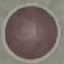

Summary:
  - Malaria status: uninfected
  - Capture: smartphone camera at the microscope eyepiece
  - Stain: Giemsa
  - Image type: automatically extracted cell patch, resized to 64 × 64 pixels
  - Preparation: thin smear